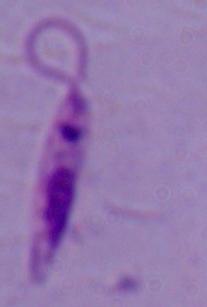
magnification = 1000x
identification = Leishmania
modality = photomicrograph